Point out each malaria parasite.
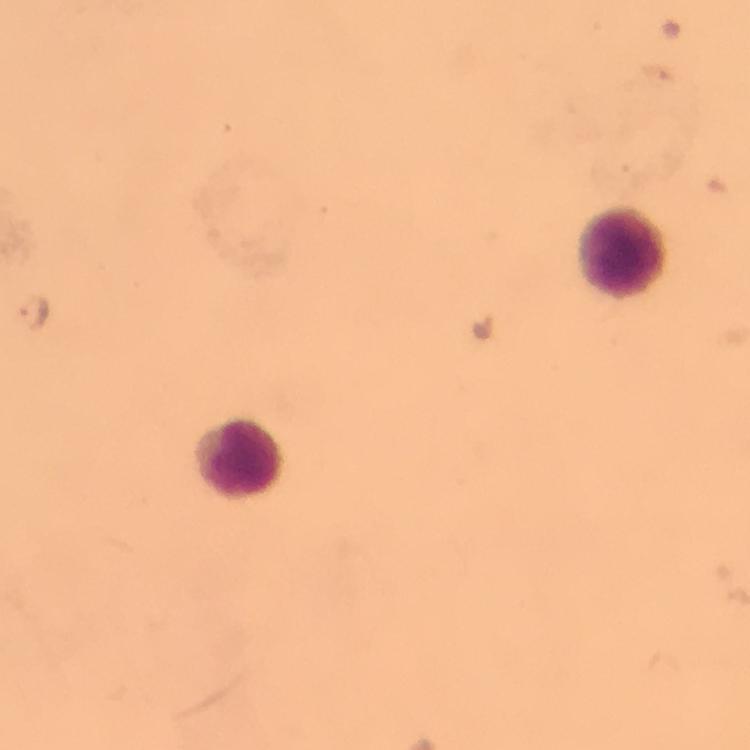
Approximate centers as [x, y] in pixels.
Malaria parasites: [36, 311].

stain = Giemsa
capture = smartphone photograph through a microscope
magnification = 100x
context = from a diagnostic examination for malaria
leukocyte locations = approximate centers as [x, y] in pixels: [621, 250], [243, 456]
preparation = thick blood smear
immersion oil = used
cropped from = one field of view
image size = 750×750 pixels